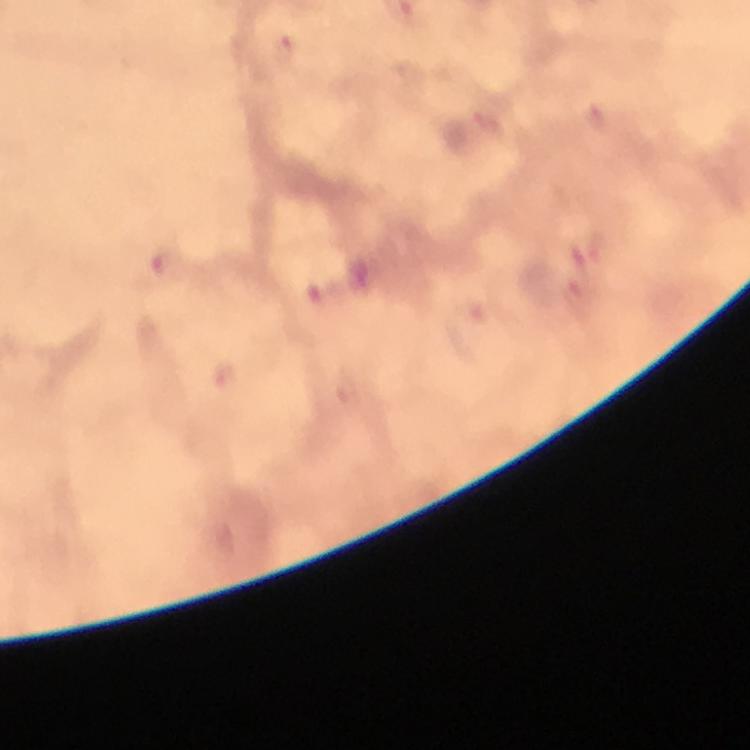

context = from a diagnostic examination for malaria
image size = 750×750 pixels
magnification = 100x
immersion oil = applied
preparation = thick blood smear
capture = smartphone camera through the microscope
cropped from = one field of view
Plasmodium parasite locations = approximate centers as (x, y) in pixels: (286, 49), (598, 116), (163, 265), (579, 299), (223, 375)
stain = Giemsa